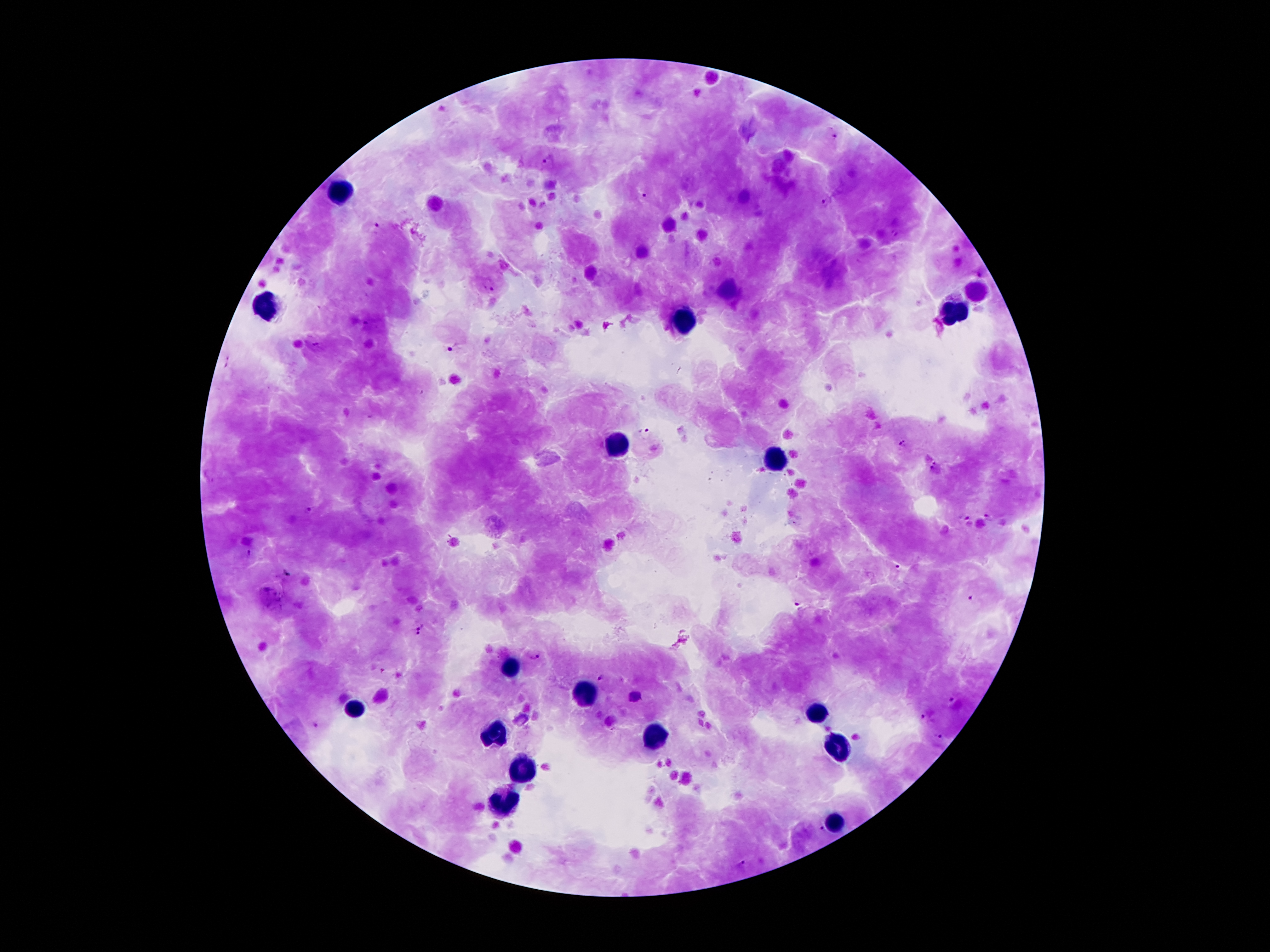

Approximate object centers, in pixels from the top-left corner.
Summary:
  - Leukocyte locations: (x=341, y=193), (x=268, y=307), (x=955, y=315), (x=684, y=323), (x=612, y=445), (x=777, y=459), (x=506, y=666), (x=588, y=697), (x=350, y=709), (x=818, y=714), (x=498, y=735), (x=652, y=738), (x=840, y=748), (x=519, y=770), (x=502, y=802), (x=834, y=824)
  - Plasmodium parasite locations: (x=835, y=136), (x=549, y=161), (x=642, y=195), (x=826, y=202), (x=376, y=225), (x=981, y=271), (x=488, y=286), (x=454, y=348), (x=228, y=363), (x=645, y=432), (x=904, y=443), (x=935, y=468), (x=307, y=511), (x=963, y=516), (x=989, y=516), (x=247, y=552), (x=897, y=567), (x=286, y=575), (x=972, y=598), (x=797, y=604), (x=417, y=621), (x=417, y=636), (x=535, y=657), (x=601, y=678), (x=953, y=701), (x=925, y=717), (x=317, y=725), (x=939, y=736), (x=821, y=830), (x=743, y=863)
  - Magnification: 100x
  - Image size: 1270×952 pixels
  - Patient malaria status: infected with Plasmodium falciparum
  - Field of view: single
  - Preparation: thick blood film
  - Stain: Giemsa
  - Capture: smartphone through the microscope eyepiece